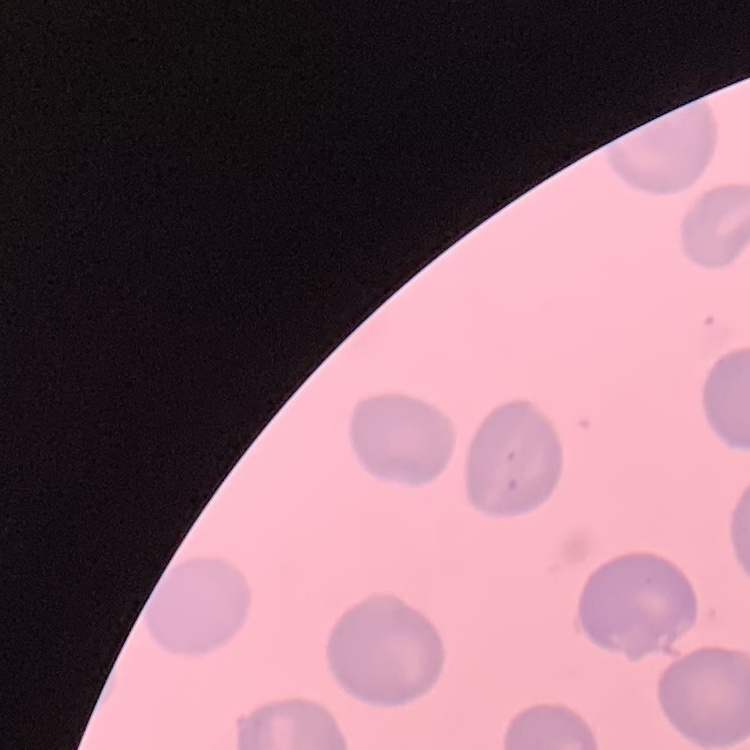

Summary:
  - Red blood cell morphology: no rouleaux formation
  - Preparation: thin blood smear
  - Image type: square crop of a larger photomicrograph
  - Stain: Field's or Giemsa